State the preparation type.
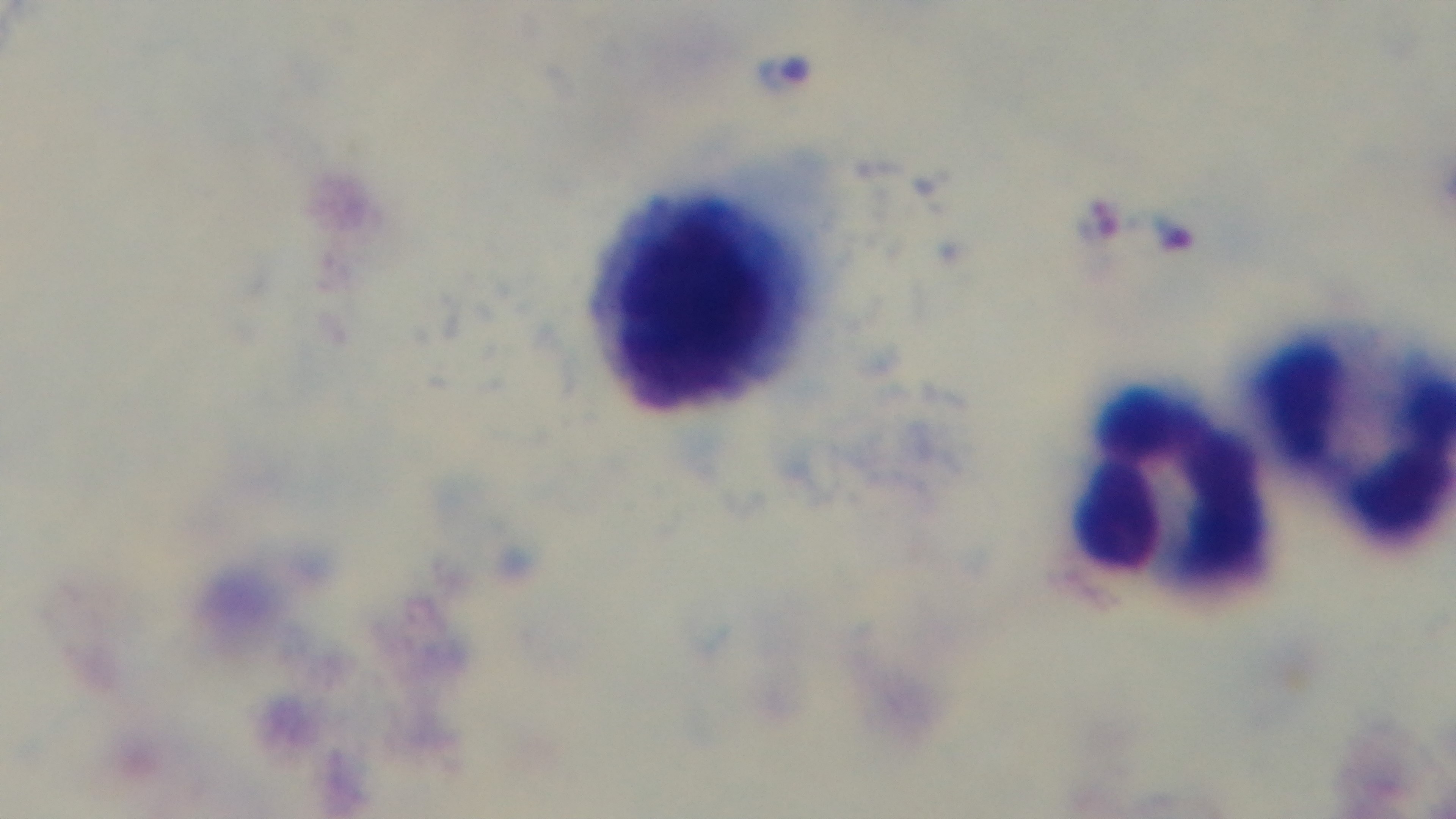

Thick.

Giemsa-stained. Photomicrograph. 100x oil-immersion objective. Single field of view. Mounted 4K digital camera. Malaria status: infected.